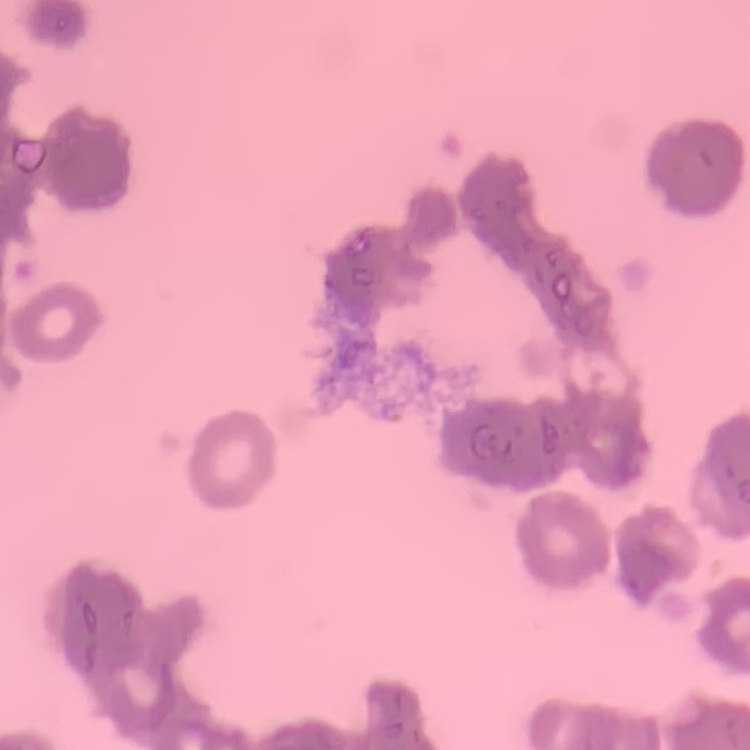

{
  "erythrocyte_morphology": "rouleaux formation",
  "image_type": "square crop of a larger photomicrograph",
  "preparation": "thin blood smear",
  "stain": "Field's or Giemsa"
}